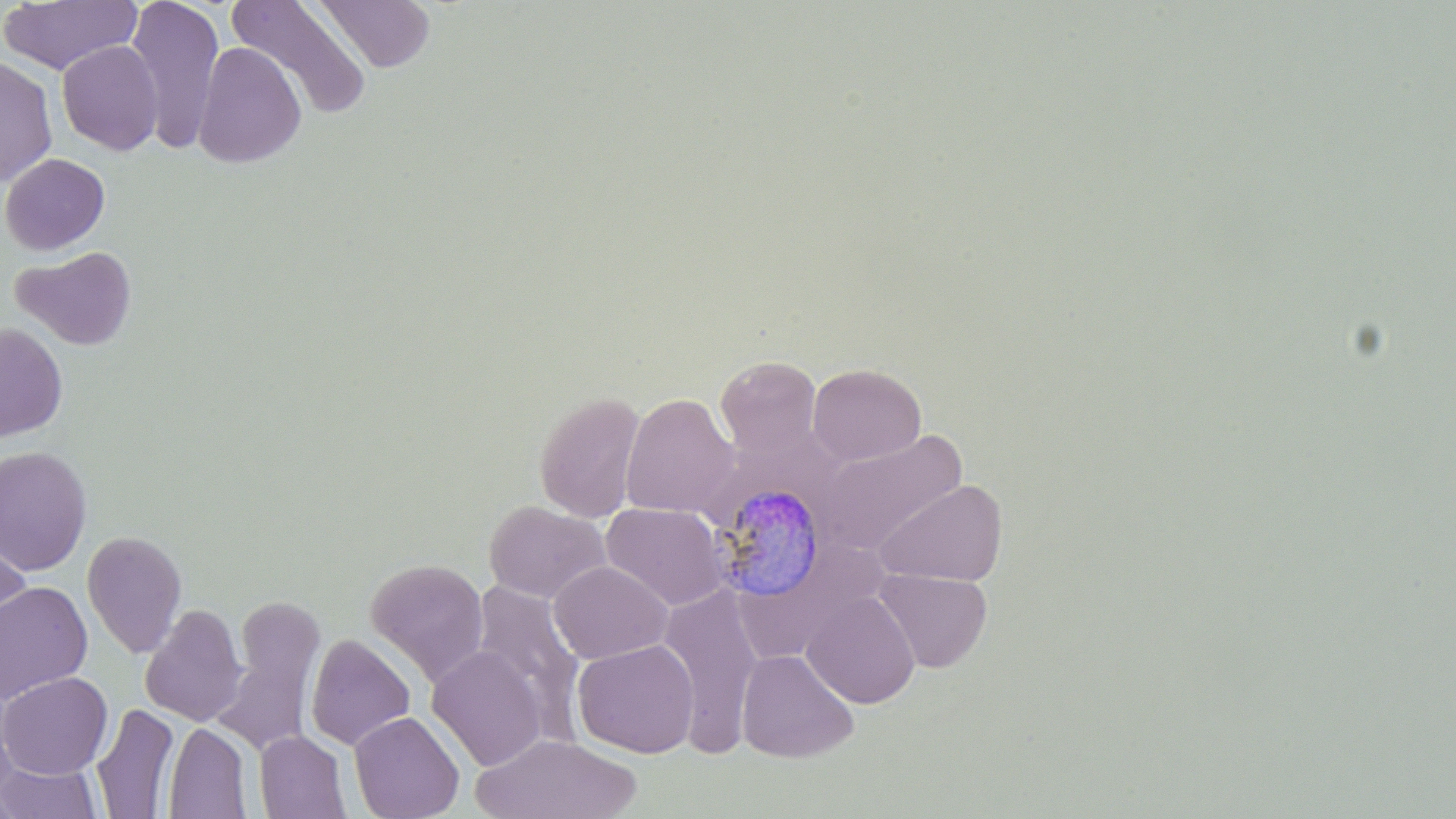

Approximate bounding boxes as named x1/y1/x2/y2 corners in pixels. Plasmodium malariae-infected red blood cell locations: (x1=711, y1=482, x2=827, y2=604). Uninfected red blood cell locations: (x1=0, y1=0, x2=142, y2=76), (x1=125, y1=0, x2=225, y2=152), (x1=226, y1=0, x2=372, y2=120), (x1=313, y1=0, x2=437, y2=73), (x1=56, y1=40, x2=164, y2=156), (x1=192, y1=42, x2=307, y2=168), (x1=0, y1=55, x2=58, y2=187), (x1=0, y1=153, x2=110, y2=255), (x1=12, y1=245, x2=137, y2=350), (x1=0, y1=323, x2=68, y2=441), (x1=715, y1=355, x2=821, y2=458), (x1=808, y1=363, x2=926, y2=465), (x1=534, y1=391, x2=646, y2=522), (x1=621, y1=393, x2=739, y2=519), (x1=815, y1=429, x2=968, y2=555), (x1=0, y1=445, x2=93, y2=575), (x1=874, y1=479, x2=1008, y2=588), (x1=484, y1=500, x2=610, y2=603), (x1=601, y1=503, x2=731, y2=610), (x1=1, y1=529, x2=31, y2=649), (x1=82, y1=530, x2=187, y2=658), (x1=365, y1=558, x2=489, y2=686), (x1=548, y1=560, x2=673, y2=664), (x1=873, y1=569, x2=993, y2=674), (x1=470, y1=579, x2=585, y2=730), (x1=0, y1=581, x2=93, y2=704), (x1=658, y1=583, x2=765, y2=756), (x1=802, y1=591, x2=920, y2=708), (x1=213, y1=596, x2=325, y2=754), (x1=140, y1=604, x2=247, y2=727), (x1=305, y1=634, x2=416, y2=751), (x1=572, y1=639, x2=699, y2=758), (x1=426, y1=646, x2=548, y2=771), (x1=737, y1=649, x2=859, y2=763), (x1=0, y1=671, x2=112, y2=780), (x1=91, y1=703, x2=180, y2=819), (x1=348, y1=710, x2=465, y2=819), (x1=163, y1=722, x2=252, y2=818), (x1=254, y1=731, x2=351, y2=818), (x1=472, y1=733, x2=643, y2=819), (x1=1, y1=761, x2=102, y2=818). Slide-level diagnosis: Plasmodium malariae. Single field of view. Thin blood smear. May-Grünwald-Giemsa stain. Optical microscopy. Captured at 1000x magnification. Image is 1456×819 pixels.